Classify this cell by malaria status.
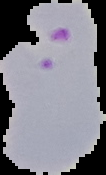
It is parasitized.

From a thin blood smear. Image is 106×175 pixels. Segmented cell region on a black background.